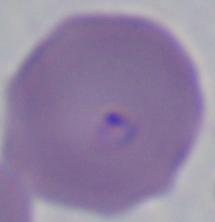

modality = micrograph
magnification = 1000x
identification = Babesia